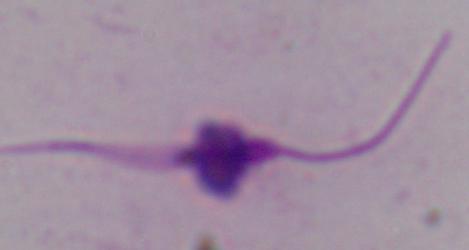

Summary:
  - Magnification: 1000x
  - Modality: photomicrograph
  - Identification: Leishmania